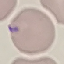

Summary:
  - Malaria status: uninfected
  - Capture: smartphone camera at the microscope eyepiece
  - Preparation: thin smear
  - Image type: cell patch, automatically extracted from a larger field of view and resized to 64 × 64 pixels
  - Stain: Giemsa